State which parasite is depicted.
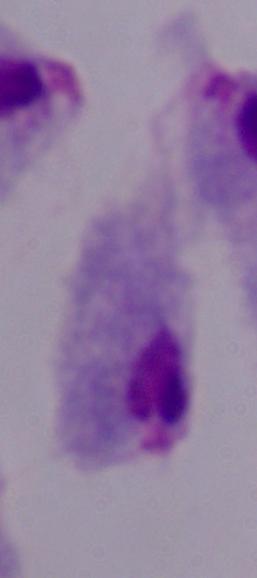

A trichomonad.

Summary:
  - Magnification: 1000x
  - Modality: photomicrograph